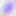
400x magnification. Toxoplasma gondii is seen. Micrograph.